Outline every Plasmodium parasite.
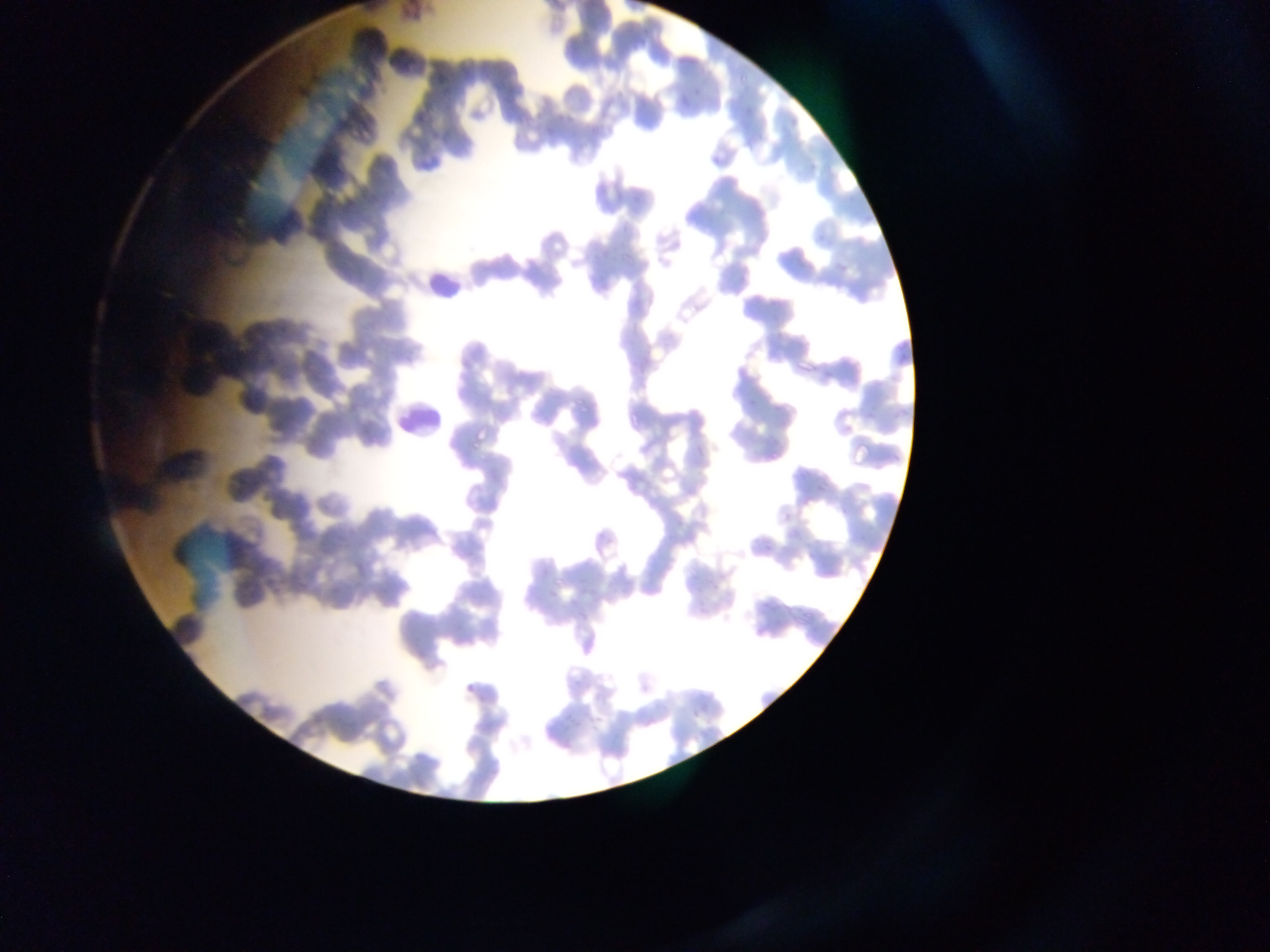

No Plasmodium parasites observed.

capture = mobile-phone photograph through a microscope
image size = 1270×952 pixels
preparation = thin blood film
country = Ghana
leukocyte locations = approximate bounding boxes as (left, top, right, bottom) in pixels: (421, 281, 459, 315), (379, 399, 446, 450)
field of view = single